Name the blood parasite species.
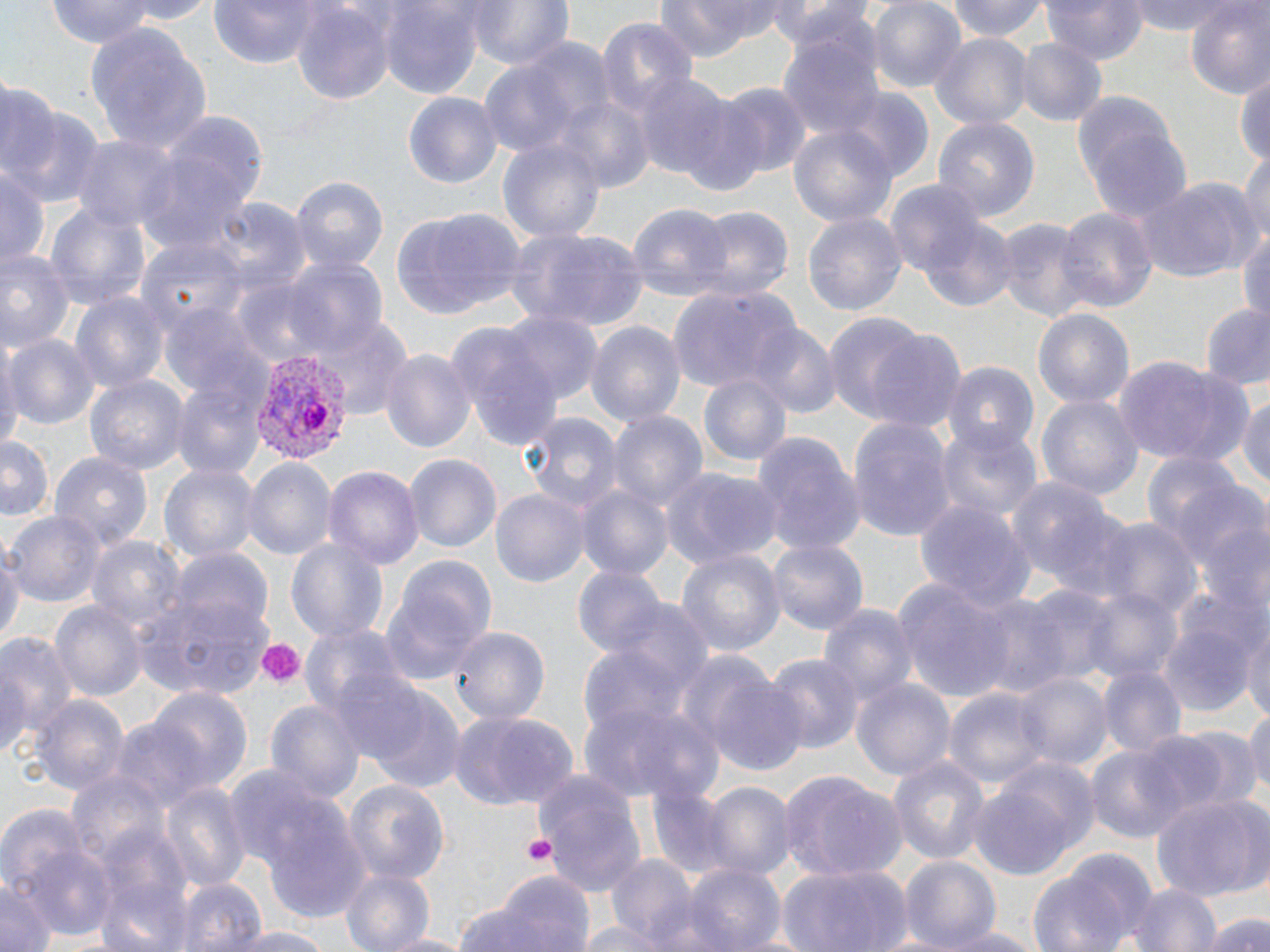

Plasmodium vivax.

modality = optical microscopy
stain = May-Grünwald-Giemsa
Plasmodium vivax-infected red blood cell locations = approximate bounding boxes as (x1, y1, x2, y2) in pixels: (246, 349, 350, 462)
image size = 1270×952 pixels
field of view = single
preparation = thin blood smear
platelet locations = approximate bounding boxes as (x1, y1, x2, y2) in pixels: (256, 638, 304, 686), (523, 834, 557, 866)
magnification = 1000x
uninfected red blood cell locations = approximate bounding boxes as (x1, y1, x2, y2) in pixels: (45, 0, 160, 50), (207, 0, 328, 67), (468, 0, 574, 71), (655, 0, 790, 58), (867, 0, 967, 93), (947, 0, 1052, 42), (1043, 0, 1146, 64), (1131, 0, 1244, 37), (1183, 0, 1270, 100), (382, 1, 483, 99), (766, 2, 871, 52), (292, 3, 393, 103), (598, 18, 697, 114), (84, 21, 214, 157), (779, 28, 886, 144), (929, 33, 1030, 129), (1014, 37, 1107, 128), (483, 39, 614, 158), (1235, 70, 1270, 172), (631, 71, 735, 181), (712, 79, 814, 179), (0, 82, 61, 185), (1074, 88, 1190, 217), (836, 90, 936, 184), (404, 93, 501, 187), (551, 95, 653, 192), (673, 96, 776, 199), (8, 105, 106, 210), (932, 114, 1040, 222), (789, 124, 898, 227), (69, 133, 180, 235), (497, 135, 605, 246), (134, 137, 261, 258), (1239, 154, 1270, 249), (0, 163, 48, 275), (1138, 175, 1261, 284), (290, 176, 388, 274), (885, 180, 985, 280), (44, 199, 152, 311), (206, 200, 309, 298), (626, 204, 733, 299), (690, 205, 794, 300), (1055, 206, 1157, 315), (390, 209, 520, 323), (801, 210, 907, 321), (921, 217, 1019, 313), (992, 219, 1094, 323), (1238, 223, 1270, 323), (505, 227, 651, 331), (137, 237, 246, 331), (0, 248, 75, 356), (283, 258, 389, 359), (669, 284, 801, 396), (69, 291, 169, 396), (1195, 302, 1270, 390), (161, 304, 268, 403), (1034, 308, 1133, 416), (820, 309, 939, 427), (499, 311, 602, 407), (308, 317, 411, 415), (584, 319, 689, 429), (743, 321, 841, 417), (449, 327, 560, 453), (865, 330, 968, 434), (5, 331, 101, 429), (379, 346, 477, 455), (1112, 355, 1254, 468), (942, 362, 1037, 451), (699, 374, 792, 471), (85, 375, 188, 479), (170, 378, 267, 481), (1036, 391, 1142, 503), (1237, 392, 1270, 490), (606, 407, 708, 517), (521, 409, 624, 518), (848, 418, 954, 542), (936, 422, 1043, 527), (752, 432, 866, 555), (0, 435, 55, 520), (1140, 450, 1266, 586), (403, 452, 500, 552), (50, 453, 153, 552), (243, 457, 336, 560), (162, 461, 259, 565), (325, 464, 424, 575), (662, 465, 783, 570), (1005, 477, 1135, 602), (576, 482, 673, 585), (491, 487, 589, 588), (914, 500, 1035, 613), (7, 510, 104, 605), (1096, 517, 1199, 620), (88, 534, 184, 637), (767, 534, 868, 635), (287, 538, 388, 644), (0, 543, 22, 655), (675, 545, 784, 658), (169, 547, 272, 640), (390, 553, 498, 656), (574, 565, 669, 660), (896, 580, 1018, 704), (1023, 585, 1121, 681), (1074, 586, 1184, 685), (137, 591, 273, 697), (380, 591, 483, 686), (973, 593, 1073, 701), (1162, 593, 1265, 715), (611, 599, 714, 699), (52, 601, 143, 701), (817, 603, 919, 713), (1242, 621, 1269, 730), (300, 623, 409, 724), (448, 623, 549, 726), (0, 629, 80, 750), (578, 645, 689, 744), (766, 652, 864, 754), (1096, 661, 1186, 761), (702, 670, 812, 781), (1012, 670, 1112, 774), (851, 678, 955, 781), (946, 686, 1048, 792), (366, 688, 466, 794), (145, 689, 251, 797), (28, 695, 129, 796), (262, 697, 366, 809), (586, 700, 724, 802), (1245, 701, 1269, 809), (448, 709, 579, 810), (1174, 726, 1261, 811), (1130, 731, 1235, 829), (1085, 743, 1189, 842), (888, 755, 989, 863), (530, 769, 650, 902), (67, 770, 168, 869), (778, 772, 907, 882), (968, 774, 1088, 878), (344, 780, 450, 884), (159, 781, 249, 894), (703, 781, 793, 884), (647, 785, 735, 880), (1150, 792, 1268, 903), (261, 802, 368, 920), (0, 807, 90, 896), (24, 847, 118, 943), (1028, 849, 1159, 952), (610, 855, 698, 947), (900, 857, 999, 949), (681, 864, 786, 952), (778, 864, 913, 951), (340, 867, 435, 952), (96, 870, 196, 952), (472, 872, 597, 952), (175, 876, 264, 952), (0, 882, 54, 952), (1127, 882, 1223, 952), (1201, 911, 1267, 952), (225, 926, 336, 952), (938, 926, 1045, 951), (382, 930, 473, 952)